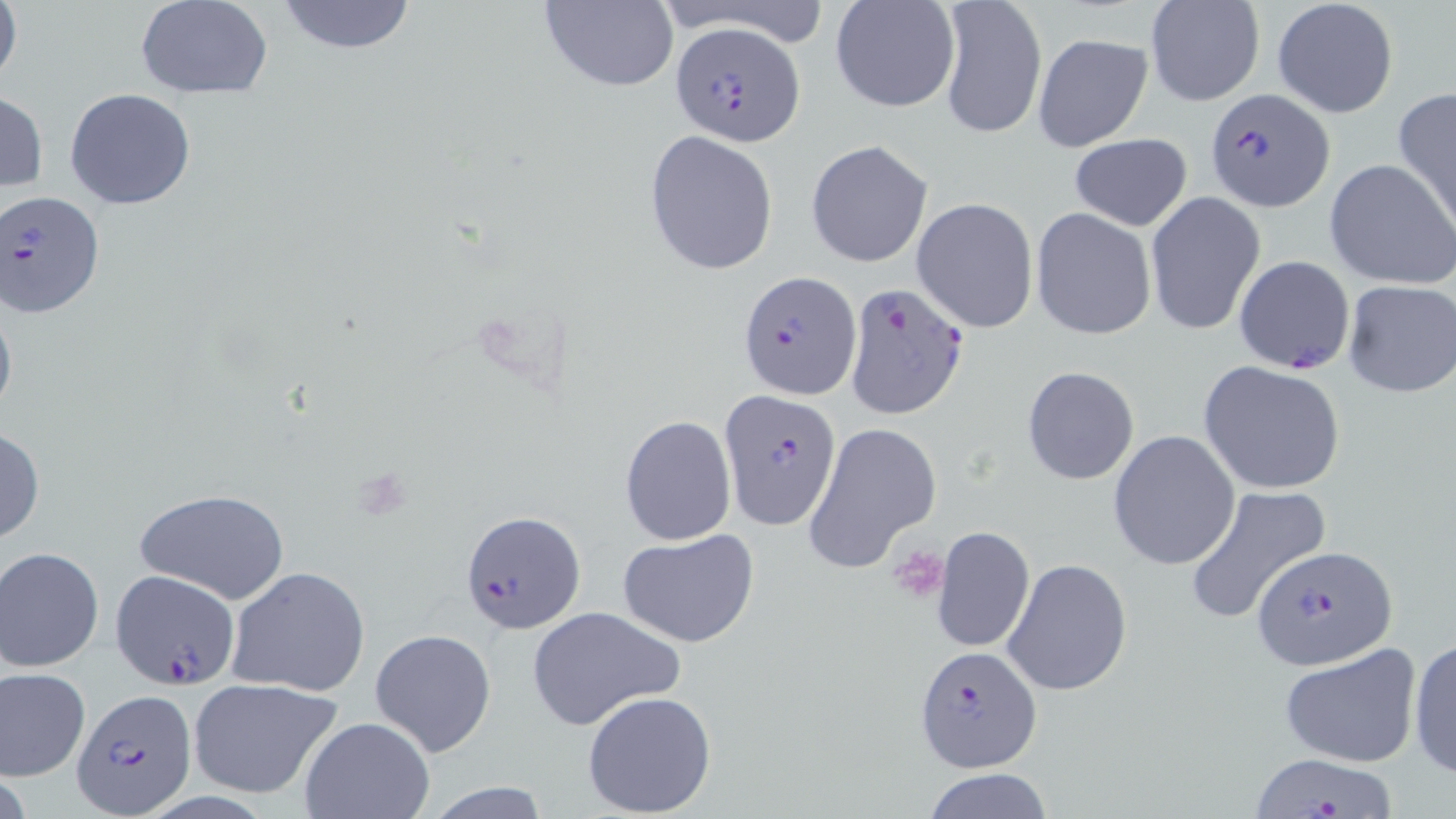
Summary:
  - Coordinate format: approximate bounding boxes as [x1, y1, x2, y2] in pixels
  - Plasmodium falciparum-infected red blood cell locations: [672, 23, 805, 146], [1205, 88, 1333, 211], [0, 191, 106, 320], [738, 268, 861, 400], [843, 284, 969, 421], [721, 389, 842, 531], [460, 509, 586, 635], [1253, 544, 1397, 671], [108, 568, 240, 689], [914, 644, 1041, 774], [68, 691, 198, 817], [1251, 752, 1396, 818]
  - Platelet locations: [890, 547, 948, 600]
  - Uninfected red blood cell locations: [0, 0, 23, 93], [136, 0, 273, 97], [274, 0, 420, 55], [538, 0, 679, 91], [937, 0, 1047, 140], [1143, 0, 1266, 106], [1271, 0, 1399, 119], [830, 1, 961, 115], [1032, 32, 1153, 152], [65, 88, 196, 210], [1393, 89, 1456, 229], [0, 90, 48, 195], [646, 130, 779, 273], [1068, 132, 1193, 231], [805, 139, 934, 269], [1325, 159, 1456, 289], [1144, 192, 1266, 336], [911, 197, 1039, 333], [1031, 206, 1157, 341], [1234, 255, 1355, 374], [1342, 279, 1456, 397], [0, 292, 17, 429], [1198, 360, 1347, 495], [1022, 367, 1140, 484], [620, 415, 737, 546], [803, 420, 943, 573], [0, 425, 46, 547], [1108, 430, 1240, 569], [1185, 484, 1332, 624], [133, 489, 290, 606], [930, 525, 1034, 653], [615, 528, 760, 647], [0, 546, 104, 672], [1001, 558, 1133, 697], [226, 566, 372, 698], [525, 605, 686, 731], [369, 628, 497, 759], [1408, 637, 1456, 779], [1279, 642, 1424, 768], [1, 668, 91, 780], [186, 678, 343, 799], [581, 690, 717, 816], [297, 716, 436, 819], [921, 768, 1054, 819], [418, 782, 556, 817]
  - Slide-level diagnosis: Plasmodium falciparum
  - Field of view: one of a larger specimen
  - Image size: 1456×819 pixels
  - Modality: light microscopy
  - Magnification: 1000x
  - Stain: May-Grünwald-Giemsa
  - Preparation: thin blood film